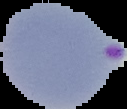

Summary:
  - Malaria status: parasitized
  - Image type: cell region segmented out of the field of view; surrounding area masked to black
  - Preparation: thin blood film
  - Image size: 127×109 pixels